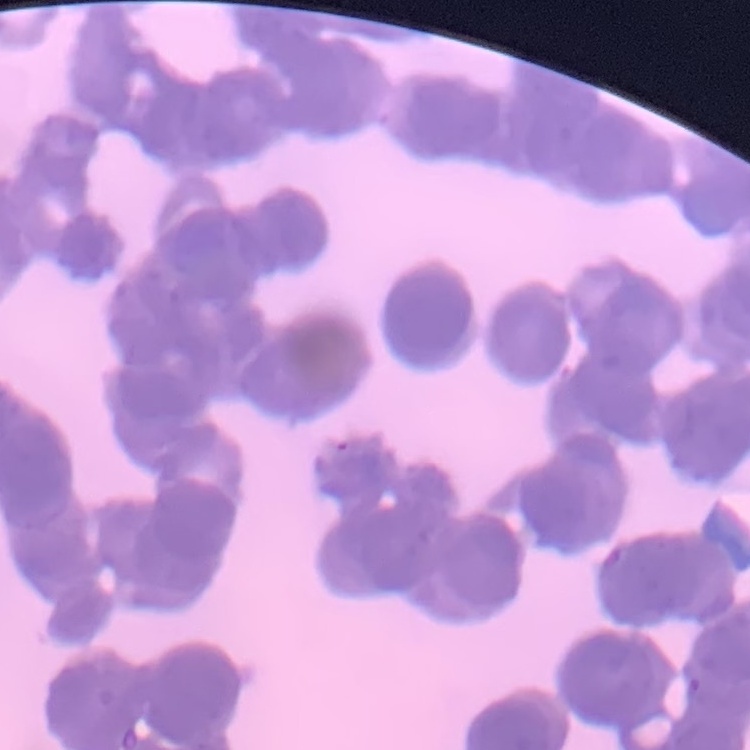

Summary:
  - Red blood cell morphology: rouleaux formation
  - Preparation: thin blood film
  - Stain: Field's or Giemsa
  - Image type: square crop of a larger photomicrograph